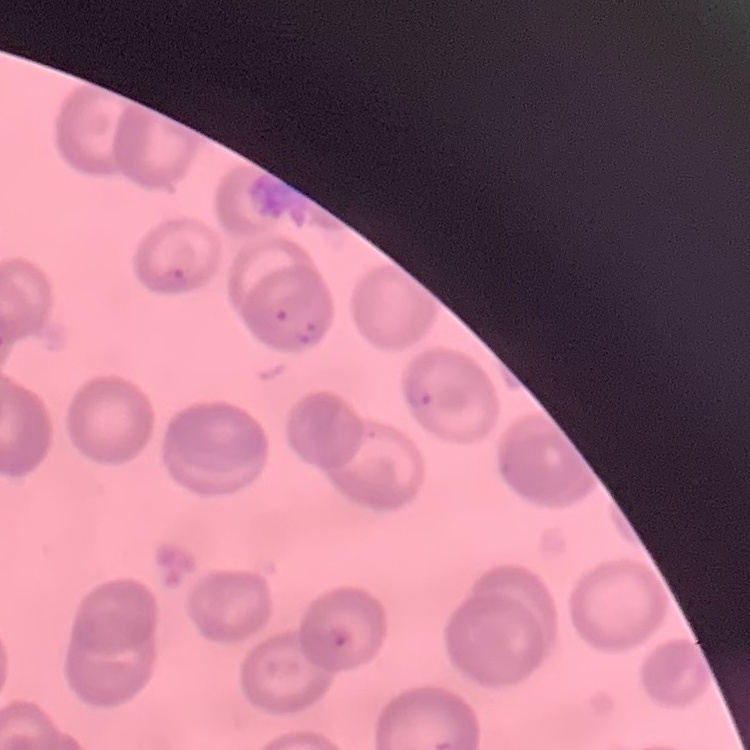

erythrocyte_morphology: no rouleaux formation
image_type: square crop of a larger photomicrograph
preparation: thin blood film
stain: Field's or Giemsa